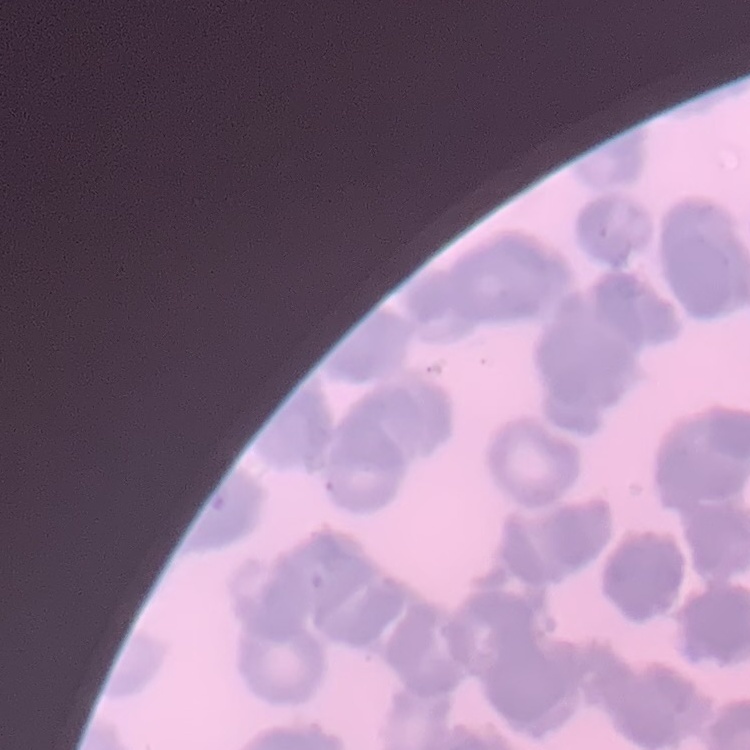

red_blood_cell_morphology: rouleaux formation
stain: Field's or Giemsa
image_type: one tile cut from a larger photomicrograph
preparation: thin peripheral smear